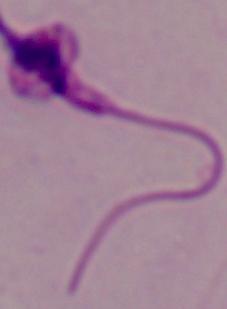

identification: Leishmania
magnification: 1000x
modality: photomicrograph